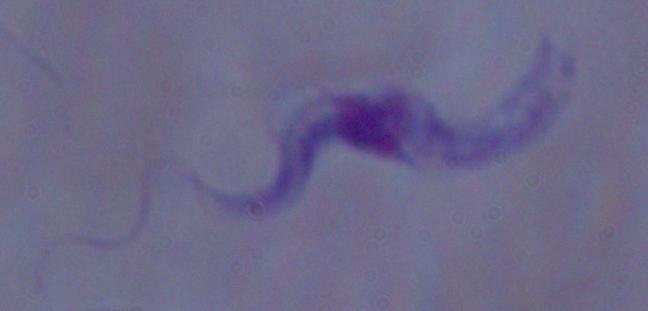

Summary:
  - Identification: trypanosome
  - Modality: photomicrograph
  - Magnification: 1000x